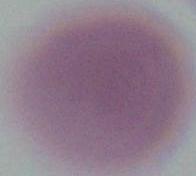

Summary:
  - Magnification: 1000x
  - Identification: red blood cell
  - Modality: micrograph